State the preparation type.
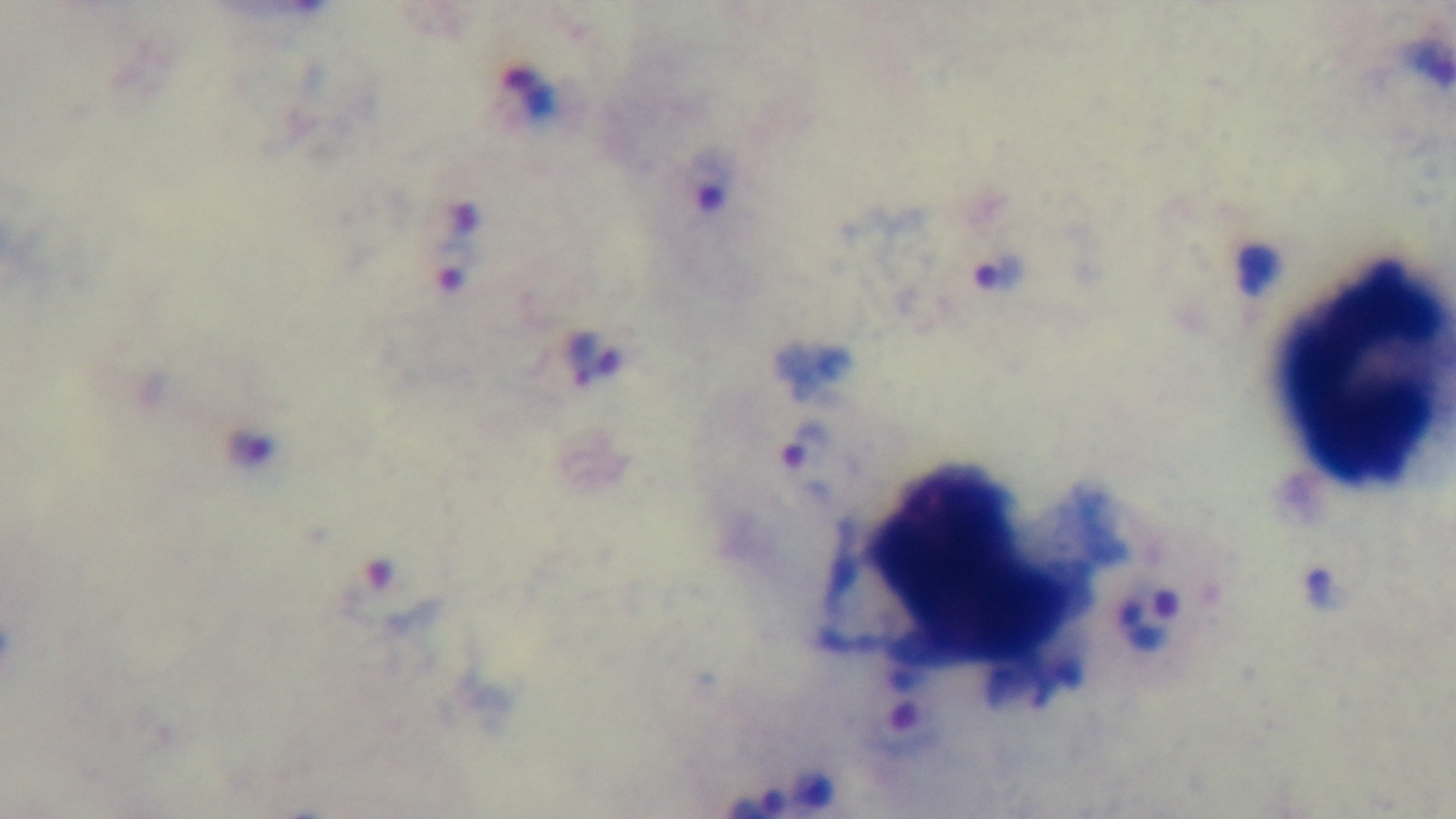

A thick smear.

field of view = one from the slide
objective = 100x oil immersion
capture = mounted 4K digital camera
stain = Giemsa
modality = light microscopy
malaria status = infected